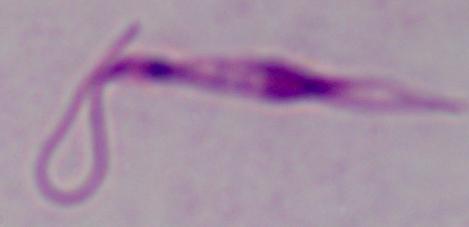

Summary:
  - Identification: Leishmania
  - Modality: photomicrograph
  - Magnification: 1000x